Name the parasite shown.
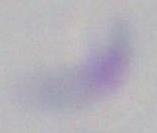

Toxoplasma gondii.

Captured at 1000x magnification. Micrograph.